Locate every blood parasite and identify its species.
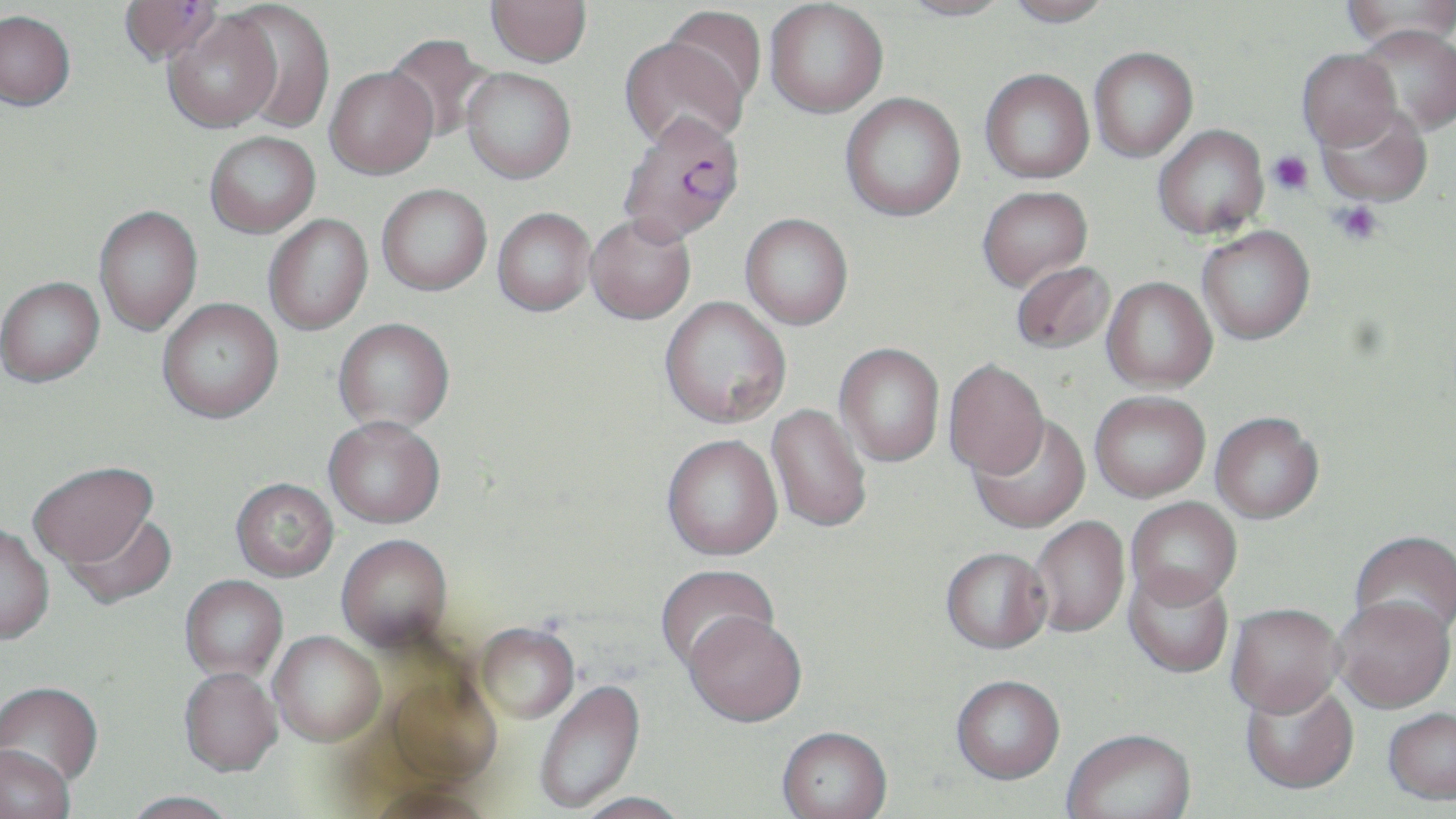
Approximate bounding boxes as (x1, y1, x2, y2) in pixels.
Plasmodium falciparum-infected red blood cells: (118, 1, 223, 66), (616, 110, 745, 244).
No Plasmodium ovale, Plasmodium malariae, Plasmodium vivax, Babesia divergens, or Trypanosoma brucei observed.

Platelet locations: (1267, 150, 1313, 195), (1331, 200, 1384, 245). Uninfected red blood cell locations: (486, 0, 592, 67), (897, 0, 1013, 21), (1005, 0, 1113, 27), (1340, 0, 1456, 51), (764, 1, 888, 118), (223, 2, 336, 133), (663, 7, 765, 111), (0, 10, 75, 110), (162, 12, 280, 133), (1355, 24, 1456, 135), (383, 34, 498, 143), (619, 36, 749, 152), (1089, 47, 1198, 162), (1296, 49, 1400, 150), (325, 67, 438, 179), (461, 68, 576, 184), (980, 68, 1094, 183), (840, 93, 966, 222), (1317, 104, 1433, 206), (1153, 124, 1268, 239), (204, 131, 320, 237), (377, 184, 491, 295), (977, 185, 1092, 292), (94, 206, 202, 336), (492, 207, 595, 315), (740, 213, 853, 330), (586, 214, 696, 325), (263, 215, 372, 335), (1197, 226, 1315, 344), (1010, 261, 1114, 355), (0, 276, 104, 387), (1102, 276, 1217, 392), (659, 296, 791, 429), (157, 298, 283, 424), (333, 318, 455, 433), (834, 343, 944, 467), (943, 360, 1049, 481), (1090, 391, 1210, 503), (766, 404, 872, 535), (1210, 414, 1324, 526), (970, 417, 1090, 535), (324, 419, 446, 531), (661, 437, 782, 564), (28, 464, 159, 572), (230, 480, 338, 583), (1125, 499, 1242, 613), (59, 513, 177, 610), (1029, 517, 1129, 640), (0, 527, 55, 648), (1349, 532, 1456, 645), (336, 537, 454, 656), (940, 550, 1053, 657), (656, 566, 779, 675), (1122, 570, 1234, 680), (179, 577, 288, 683), (1332, 600, 1455, 716), (1226, 607, 1344, 723), (683, 618, 807, 731), (476, 625, 580, 726), (268, 633, 385, 750), (178, 671, 282, 779), (382, 675, 501, 793), (951, 678, 1065, 788), (535, 681, 647, 814), (1240, 681, 1359, 798), (0, 684, 104, 794), (1383, 710, 1456, 809), (776, 730, 893, 819), (1062, 732, 1197, 819), (1, 748, 75, 819), (363, 787, 498, 819), (120, 793, 239, 819), (571, 794, 692, 819). Slide-level diagnosis: Plasmodium falciparum. Image is 1456×819 pixels. Captured at 1000x magnification. Thin blood film. One field of a larger specimen. Optical microscopy. May-Grünwald-Giemsa-stained preparation.